State which parasite is depicted.
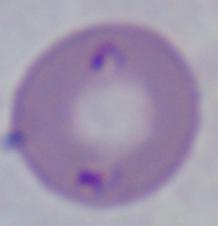
Babesia.

Summary:
  - Modality: photomicrograph
  - Magnification: 1000x